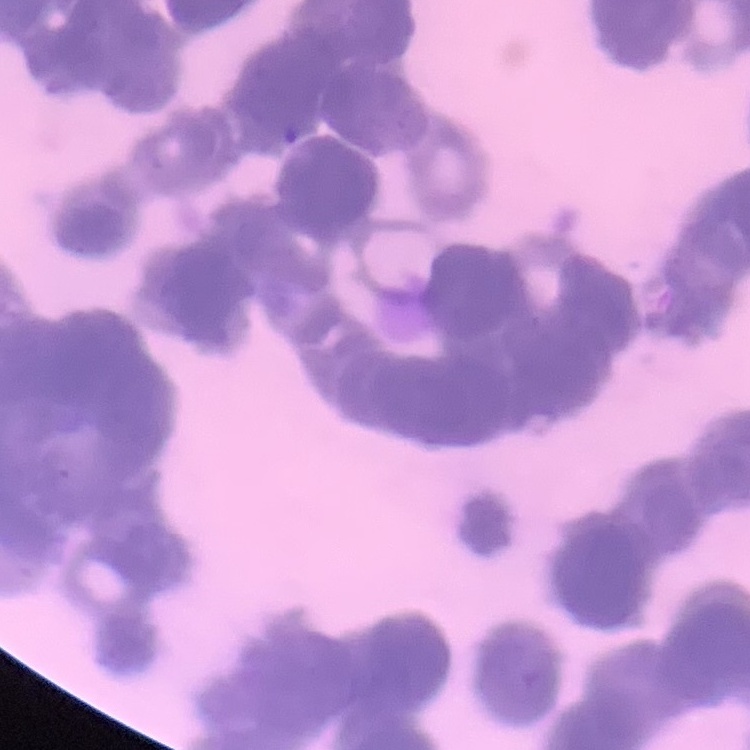
erythrocyte morphology = rouleaux formation
preparation = thin blood smear
stain = Field's or Giemsa
image type = one tile cut from a larger photomicrograph